Give the extent of all Plasmodium vivax-infected red blood cells.
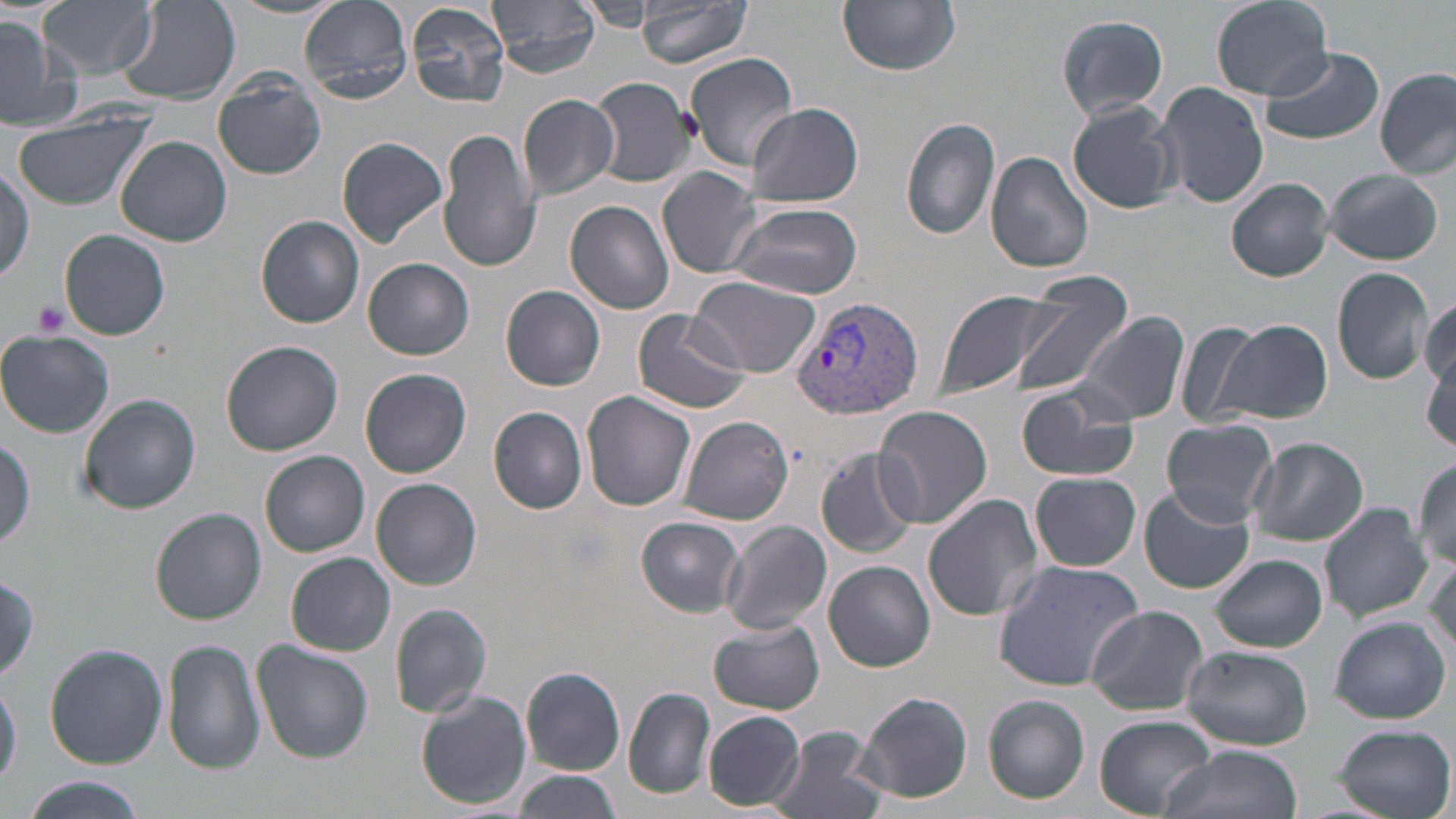
Approximate bounding boxes as [x1, y1, x2, y2] in pixels.
Plasmodium vivax-infected red blood cells: [788, 296, 924, 423].

Summary:
  - Uninfected red blood cell locations: [39, 0, 155, 79], [228, 0, 345, 20], [300, 0, 412, 102], [489, 0, 602, 76], [635, 0, 754, 68], [839, 0, 961, 76], [1209, 0, 1334, 101], [118, 1, 241, 106], [580, 2, 652, 32], [405, 3, 511, 107], [1057, 14, 1169, 121], [0, 17, 77, 129], [1260, 45, 1384, 144], [685, 52, 799, 170], [1377, 68, 1456, 180], [212, 72, 326, 180], [587, 75, 697, 190], [1157, 81, 1269, 209], [518, 93, 620, 200], [1067, 99, 1183, 213], [746, 103, 863, 207], [7, 107, 156, 210], [900, 117, 1002, 241], [439, 130, 541, 274], [337, 135, 449, 248], [117, 136, 232, 247], [986, 151, 1095, 274], [0, 166, 33, 285], [1322, 166, 1443, 265], [657, 167, 764, 278], [1226, 178, 1334, 281], [564, 200, 676, 315], [726, 200, 863, 300], [257, 215, 366, 329], [60, 230, 171, 341], [364, 257, 474, 360], [1330, 267, 1435, 386], [691, 277, 820, 377], [1010, 278, 1134, 401], [501, 285, 605, 391], [938, 288, 1063, 399], [1419, 295, 1455, 395], [633, 307, 751, 414], [1076, 313, 1189, 426], [1220, 319, 1332, 424], [1178, 322, 1268, 430], [0, 330, 113, 437], [220, 340, 344, 456], [1424, 351, 1456, 450], [361, 368, 471, 478], [1016, 380, 1141, 482], [582, 392, 697, 513], [79, 394, 200, 514], [873, 405, 994, 531], [488, 406, 587, 514], [678, 416, 793, 526], [1161, 418, 1279, 526], [0, 434, 34, 553], [1247, 437, 1368, 546], [817, 449, 919, 558], [261, 451, 369, 557], [1411, 458, 1456, 570], [1031, 473, 1141, 571], [371, 478, 480, 590], [1139, 487, 1254, 596], [923, 494, 1043, 624], [1318, 503, 1432, 623], [152, 508, 266, 624], [637, 517, 746, 617], [721, 521, 832, 637], [1426, 550, 1456, 659], [286, 552, 395, 655], [1211, 554, 1328, 652], [992, 560, 1144, 688], [824, 561, 934, 672], [0, 574, 40, 682], [389, 604, 493, 718], [1085, 606, 1210, 715], [1329, 616, 1450, 725], [709, 619, 825, 715], [163, 639, 265, 774], [253, 640, 374, 762], [44, 644, 168, 769], [1180, 644, 1313, 750], [520, 667, 625, 775], [0, 681, 21, 790], [624, 689, 715, 798], [856, 691, 974, 803], [416, 692, 532, 809], [983, 696, 1089, 804], [702, 710, 805, 810], [1095, 714, 1215, 816], [1331, 723, 1455, 819], [768, 727, 886, 819], [1159, 745, 1301, 819], [513, 770, 623, 815], [18, 777, 149, 818]
  - Platelet locations: [32, 299, 71, 339]
  - Slide-level diagnosis: Plasmodium vivax
  - Field of view: one of a larger specimen
  - Stain: May-Grünwald-Giemsa
  - Magnification: 1000x
  - Modality: optical microscopy
  - Preparation: thin blood film
  - Image size: 1456×819 pixels